Name the parasite shown.
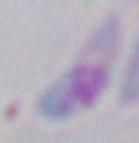

Toxoplasma gondii.

{
  "magnification": "1000x",
  "modality": "photomicrograph"
}